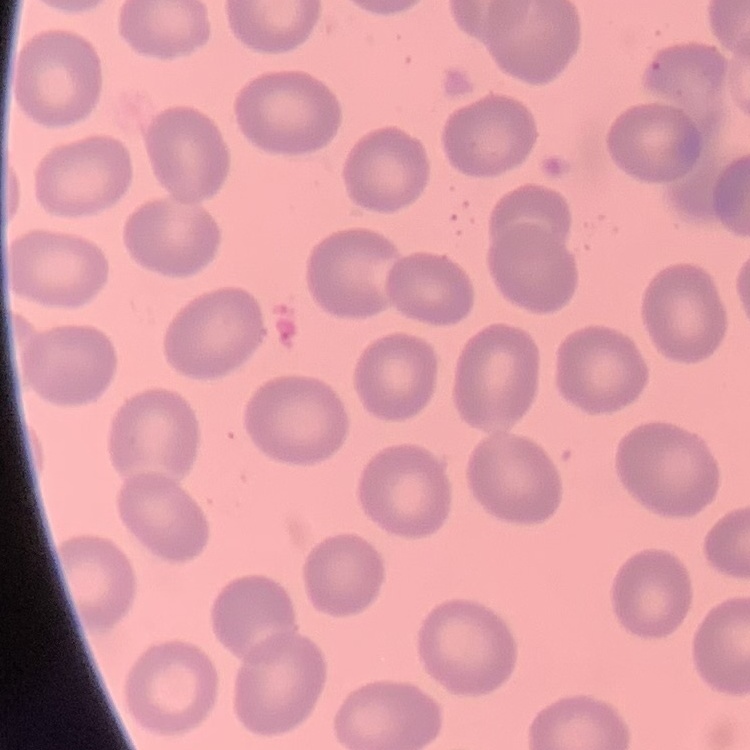

erythrocyte_morphology: no rouleaux formation
preparation: thin peripheral smear
stain: Field's or Giemsa
image_type: one tile cut from a larger photomicrograph